Give the position of every leukocyte visible.
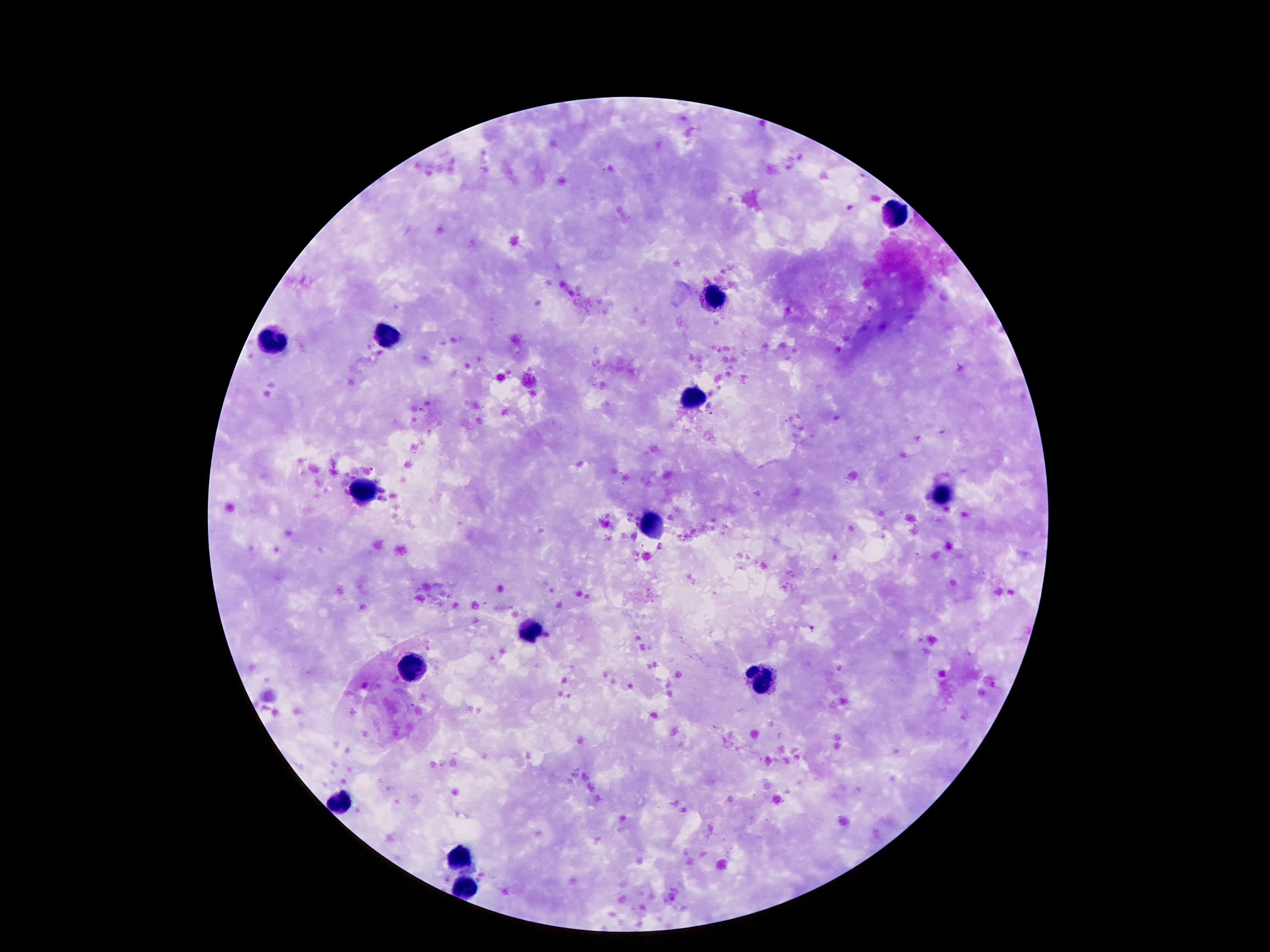

Approximate centers as (x, y) in pixels.
Leukocytes: (895, 215), (717, 297), (385, 339), (273, 343), (691, 403), (363, 491), (941, 493), (653, 526), (531, 631), (415, 666), (763, 680), (341, 802), (455, 858), (465, 890).

Image is 1270×952 pixels. 100x magnification. Photographed through the microscope eyepiece with a smartphone camera. Single field of view. Thick blood film. Giemsa-stained preparation. Patient malaria status: not infected.